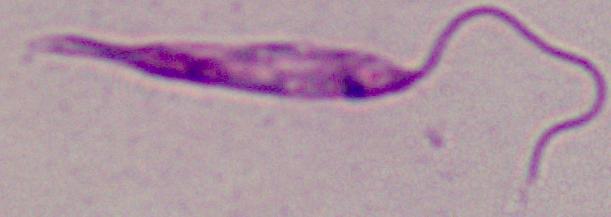
Summary:
  - Magnification: 1000x
  - Identification: Leishmania
  - Modality: micrograph